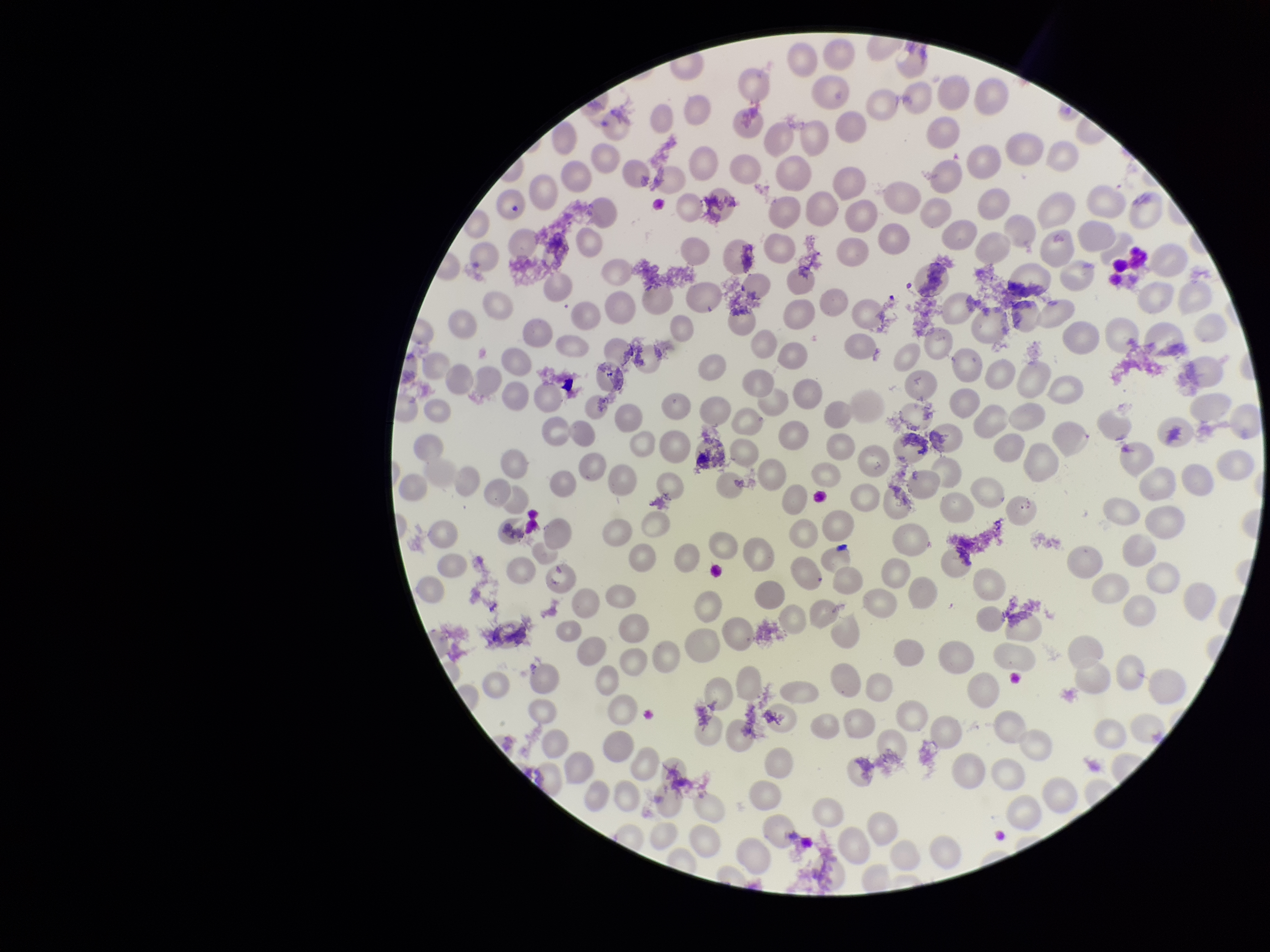
Red blood cell count: 234. Smartphone photograph taken through the eyepiece of a microscope. Parasitized red blood cell count: 0. Giemsa stain. Preparation: thin smear. Single field of view. Image is 1270×952 pixels. Patient malaria status: negative. Parasitized red blood cells: none detected.